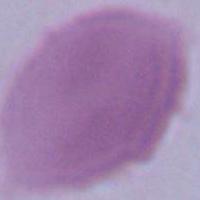
Summary:
  - Magnification: 1000x
  - Modality: photomicrograph
  - Identification: erythrocyte